Draw a bounding box around every malaria parasite, every leukocyte, and every artifact (stain precipitate or debris).
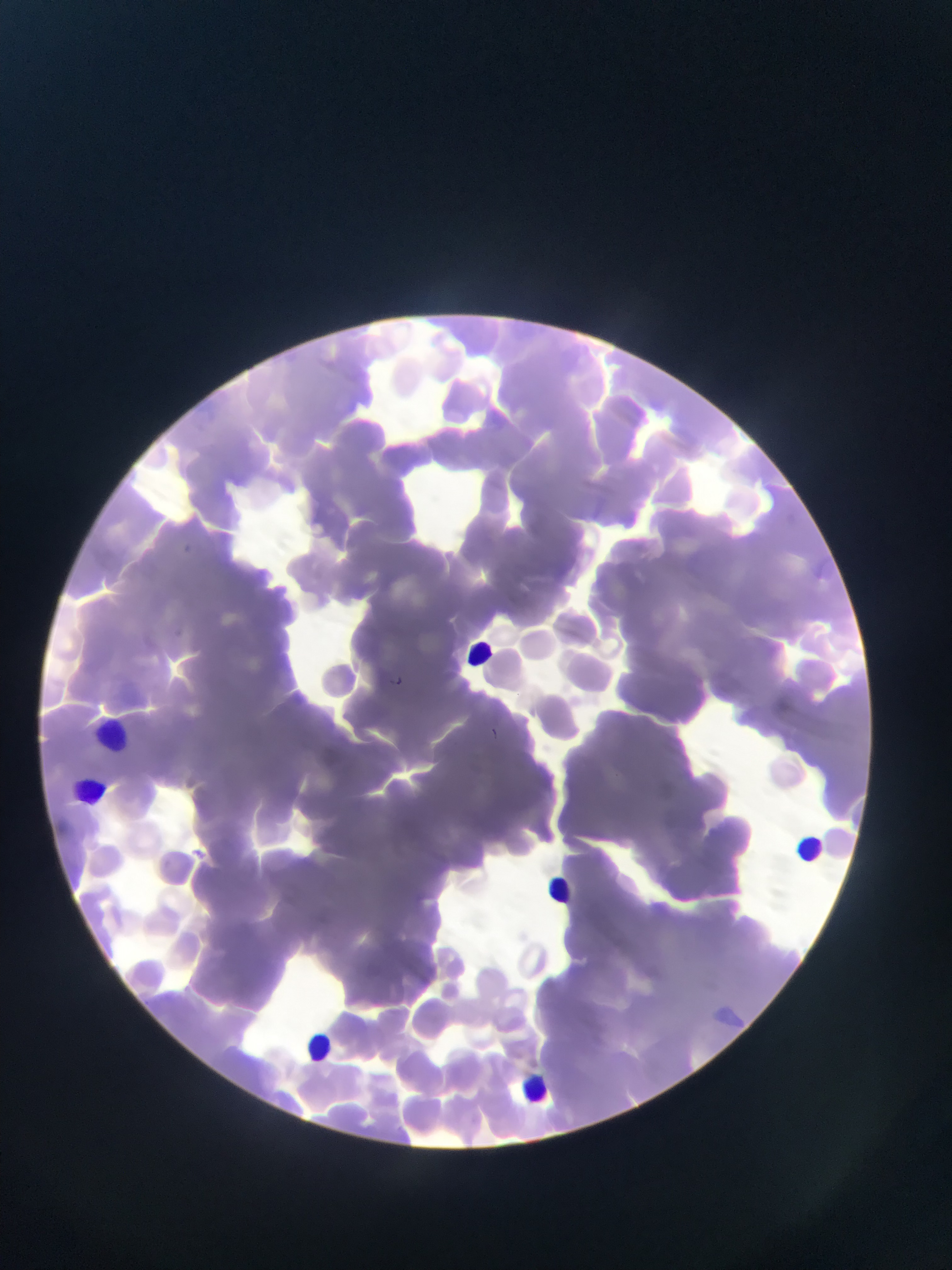

Approximate bounding boxes as {left, top, right, bottom} in pixels.
Malaria parasites: {176, 542, 202, 566}, {387, 671, 404, 686}, {483, 723, 501, 744}, {192, 840, 215, 869}.
Leukocytes: {468, 631, 494, 667}, {94, 707, 127, 757}, {76, 776, 96, 804}, {787, 832, 829, 868}, {536, 870, 583, 922}, {305, 1030, 333, 1061}, {511, 1069, 559, 1114}.

Photographed through a microscope with a mobile-phone camera. Thin blood smear. One field of view. Image is 952×1270 pixels. Sample from Ghana.